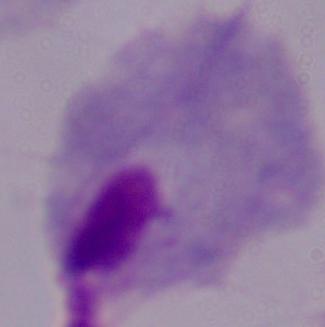

Photomicrograph. A trichomonad is seen. 1000x magnification.